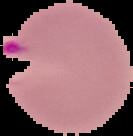 The area outside the segmented cell region is set to black. Image is 133×136 pixels. Result: malaria parasites detected. From a thin blood film.